Identify the preparation type.
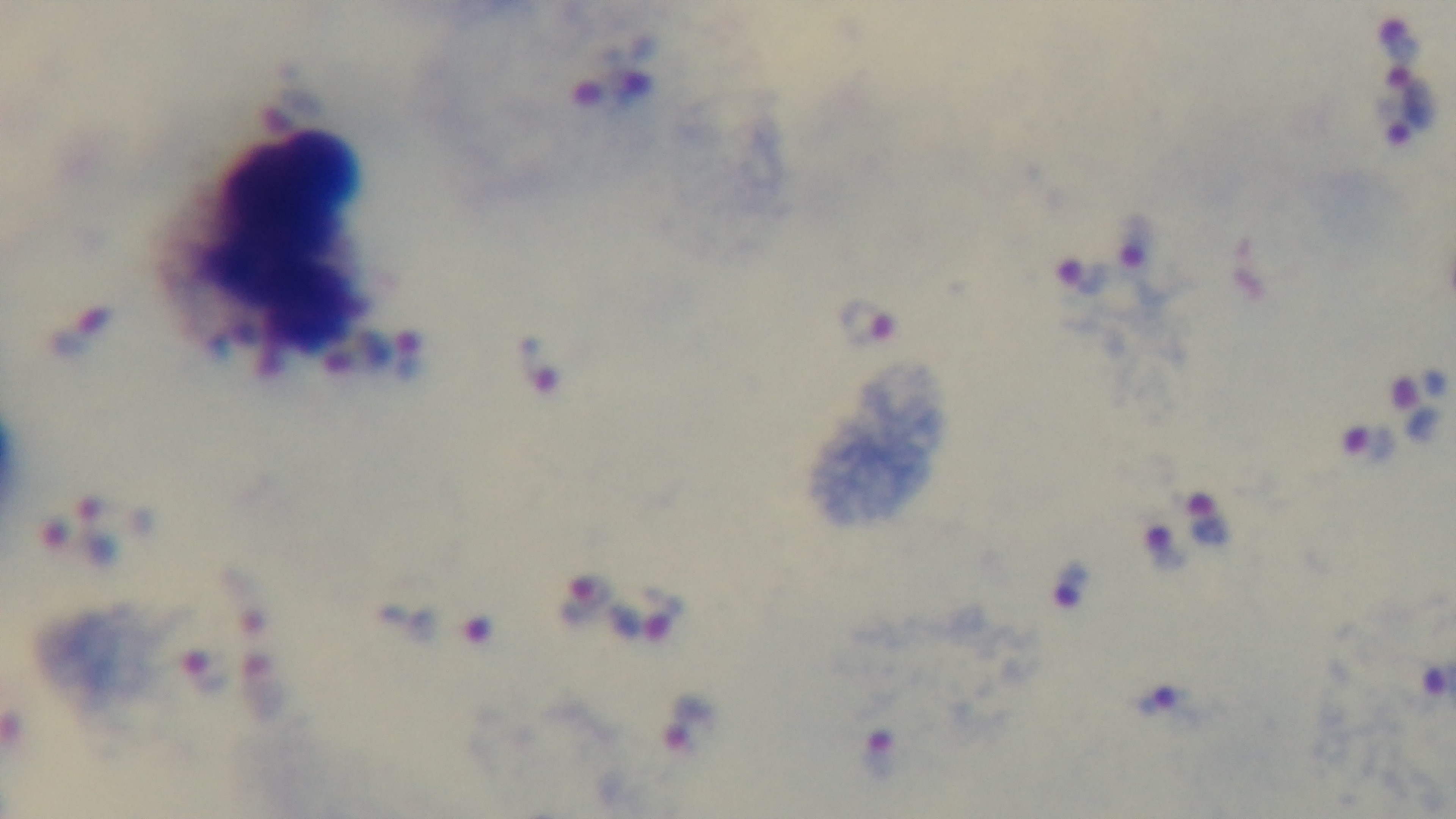

Thick.

Light microscopy. Malaria status: positive. Giemsa stain. Single field of view. Captured with a mounted 4K digital camera. 100x oil-immersion objective.